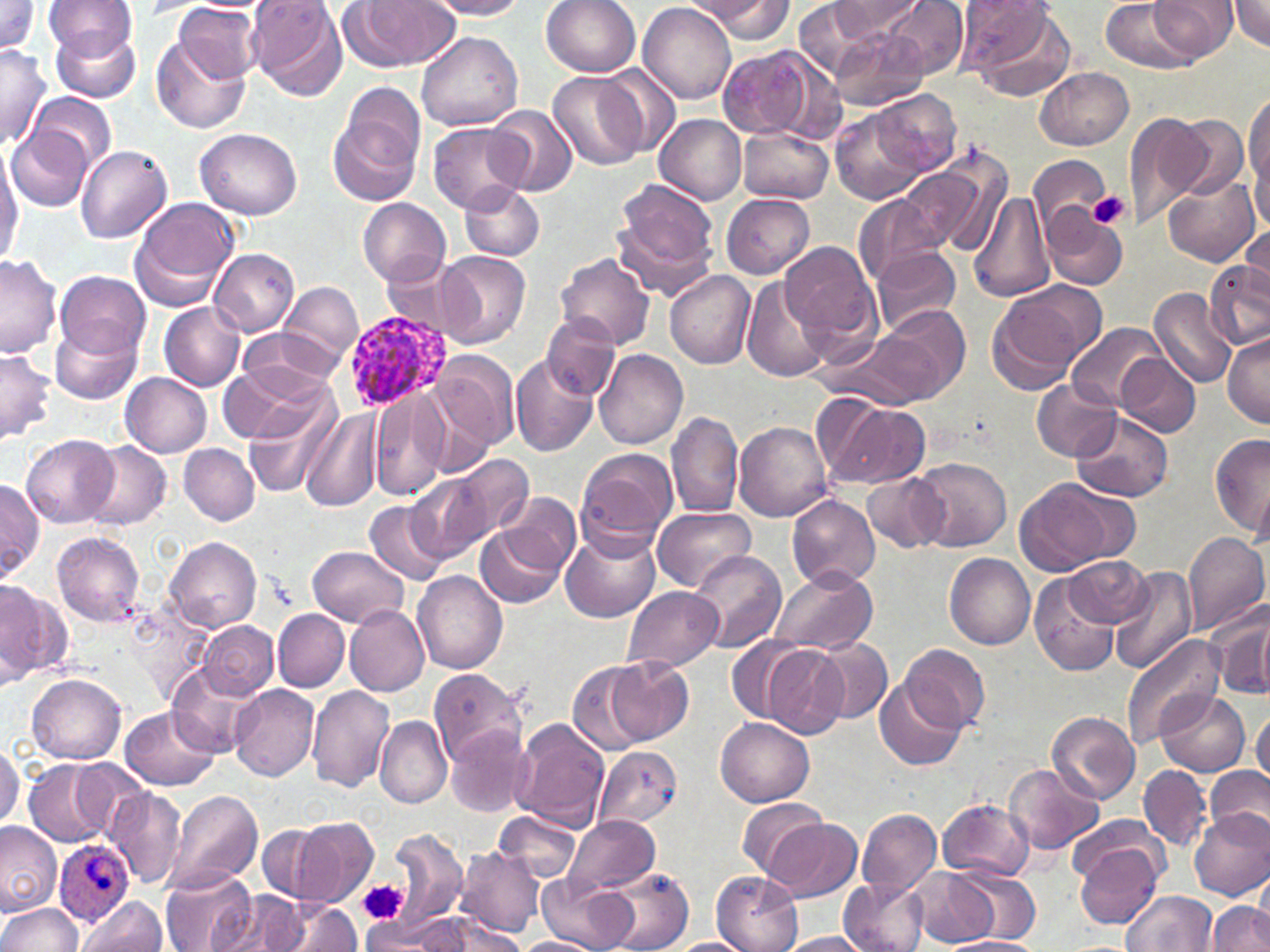
slide-level diagnosis = Plasmodium ovale
uninfected red blood cell locations = approximate bounding boxes as [x1, y1, x2, y2] in pixels: [0, 0, 40, 57], [46, 0, 136, 63], [249, 0, 347, 101], [425, 0, 529, 19], [542, 0, 642, 77], [693, 0, 795, 42], [882, 0, 968, 80], [960, 0, 1076, 100], [1101, 0, 1195, 71], [1149, 0, 1236, 61], [1230, 0, 1270, 50], [341, 1, 460, 73], [829, 1, 924, 42], [791, 2, 891, 81], [639, 3, 736, 105], [172, 4, 262, 86], [51, 22, 142, 102], [827, 24, 930, 111], [415, 32, 525, 132], [153, 34, 251, 135], [0, 41, 51, 150], [717, 47, 838, 140], [600, 66, 683, 158], [1036, 67, 1134, 151], [548, 71, 647, 170], [871, 89, 960, 177], [1244, 90, 1270, 214], [30, 92, 117, 171], [328, 103, 422, 209], [487, 106, 577, 195], [832, 110, 925, 205], [1122, 110, 1212, 229], [654, 114, 747, 206], [1173, 114, 1247, 197], [427, 122, 528, 214], [6, 125, 94, 211], [738, 126, 833, 203], [195, 127, 302, 217], [75, 144, 173, 244], [0, 145, 22, 265], [907, 148, 1013, 257], [1028, 154, 1110, 237], [1164, 171, 1259, 265], [613, 180, 721, 295], [462, 183, 544, 261], [967, 189, 1055, 302], [722, 192, 815, 278], [854, 195, 944, 289], [358, 198, 450, 288], [127, 199, 240, 310], [1044, 211, 1127, 290], [1241, 224, 1270, 302], [782, 240, 885, 353], [873, 246, 962, 335], [209, 249, 300, 337], [437, 250, 531, 350], [557, 253, 656, 349], [0, 255, 61, 359], [384, 257, 458, 334], [1205, 262, 1270, 352], [55, 270, 150, 359], [665, 271, 755, 368], [741, 277, 831, 383], [280, 281, 362, 367], [987, 283, 1098, 392], [1149, 289, 1237, 387], [158, 301, 245, 390], [859, 306, 971, 408], [541, 313, 619, 401], [50, 318, 142, 406], [1068, 323, 1169, 412], [237, 327, 345, 396], [1221, 331, 1270, 427], [431, 349, 518, 452], [0, 350, 55, 443], [595, 350, 687, 452], [511, 355, 598, 456], [1114, 355, 1200, 437], [217, 368, 320, 444], [121, 373, 212, 458], [1031, 378, 1122, 461], [245, 387, 343, 496], [371, 389, 450, 502], [823, 399, 931, 491], [300, 405, 383, 513], [667, 410, 742, 520], [1069, 410, 1174, 502], [734, 421, 834, 520], [1211, 435, 1270, 539], [22, 436, 118, 527], [83, 442, 171, 530], [180, 444, 259, 524], [575, 447, 677, 551], [446, 453, 533, 545], [913, 458, 1012, 551], [407, 471, 497, 563], [863, 473, 950, 554], [1012, 475, 1134, 576], [0, 479, 42, 580], [495, 494, 581, 577], [787, 495, 879, 593], [364, 499, 450, 584], [651, 506, 755, 592], [475, 524, 565, 608], [562, 526, 661, 625], [1182, 530, 1269, 634], [52, 531, 145, 625], [166, 535, 260, 633], [308, 545, 408, 626], [688, 549, 786, 653], [944, 551, 1035, 649], [1066, 557, 1150, 628], [769, 566, 878, 656], [1110, 566, 1197, 676], [412, 571, 508, 674], [1030, 573, 1124, 676], [0, 583, 68, 679], [621, 585, 723, 673], [1207, 598, 1270, 704], [344, 604, 428, 696], [1254, 607, 1268, 698], [272, 609, 350, 690], [199, 620, 277, 699], [726, 635, 811, 721], [812, 635, 892, 725], [1120, 635, 1222, 748], [900, 643, 990, 732], [763, 645, 845, 738], [609, 657, 695, 745], [168, 662, 259, 756], [568, 662, 653, 755], [428, 668, 529, 766], [27, 674, 126, 764], [875, 677, 967, 770], [228, 684, 318, 782], [306, 685, 397, 792], [1157, 689, 1251, 776], [122, 705, 219, 790], [1252, 710, 1270, 786], [1046, 711, 1139, 804], [715, 716, 816, 805], [376, 717, 453, 809], [513, 719, 607, 832], [444, 726, 535, 816], [0, 741, 22, 830], [593, 746, 685, 831], [24, 758, 116, 847], [72, 759, 151, 839], [1005, 763, 1104, 855], [1138, 764, 1212, 853], [1204, 766, 1270, 844], [105, 786, 186, 889], [164, 790, 263, 892], [736, 797, 830, 878], [938, 799, 1035, 881], [1187, 807, 1270, 901], [493, 809, 581, 884], [856, 809, 942, 896], [565, 813, 659, 895], [1068, 815, 1169, 887], [298, 819, 379, 905], [768, 820, 864, 902], [0, 823, 61, 915], [256, 824, 330, 901], [386, 827, 468, 934], [1075, 843, 1161, 927], [455, 846, 544, 937], [159, 865, 258, 952], [603, 867, 693, 952], [952, 867, 1041, 942], [911, 868, 999, 947], [537, 870, 634, 952], [712, 872, 803, 952], [1253, 877, 1270, 945], [838, 878, 930, 952], [212, 890, 312, 952], [1121, 890, 1215, 952], [78, 897, 166, 952], [273, 899, 361, 951], [0, 901, 85, 952], [1208, 901, 1270, 951], [411, 912, 526, 951], [360, 914, 451, 951], [776, 932, 872, 951], [668, 937, 754, 952], [949, 937, 1043, 952], [517, 938, 595, 952]
modality = optical microscopy
image size = 1270×952 pixels
field of view = single
magnification = 1000x
platelet locations = approximate bounding boxes as [x1, y1, x2, y2] in pixels: [1088, 191, 1129, 230], [359, 880, 408, 925]
Plasmodium ovale-infected red blood cell locations = approximate bounding boxes as [x1, y1, x2, y2] in pixels: [345, 313, 450, 410], [53, 840, 136, 925]
preparation = thin blood smear
stain = May-Grünwald-Giemsa